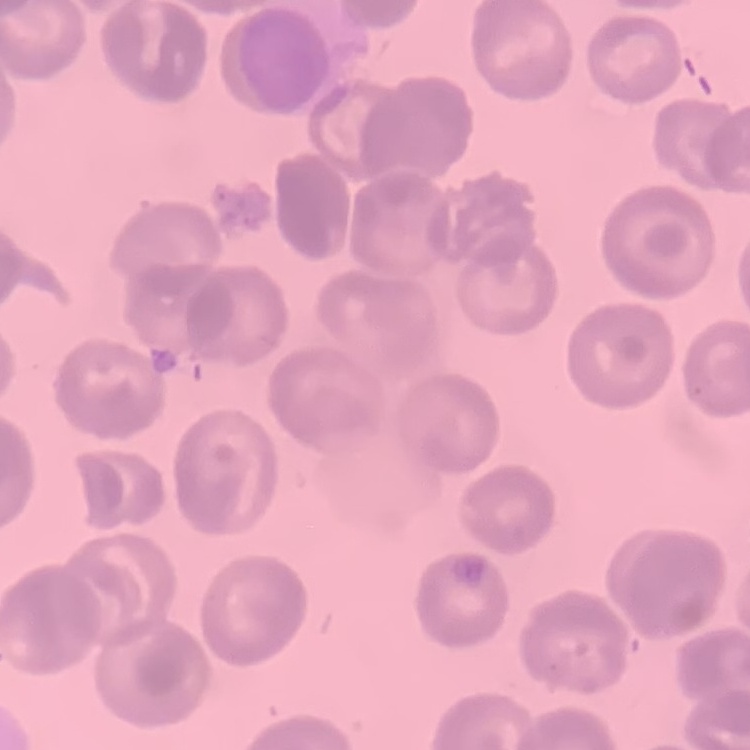

erythrocyte_morphology: no rouleaux formation
preparation: thin blood film
image_type: square crop of a larger photomicrograph
stain: Field's or Giemsa